Identify the blood parasite species.
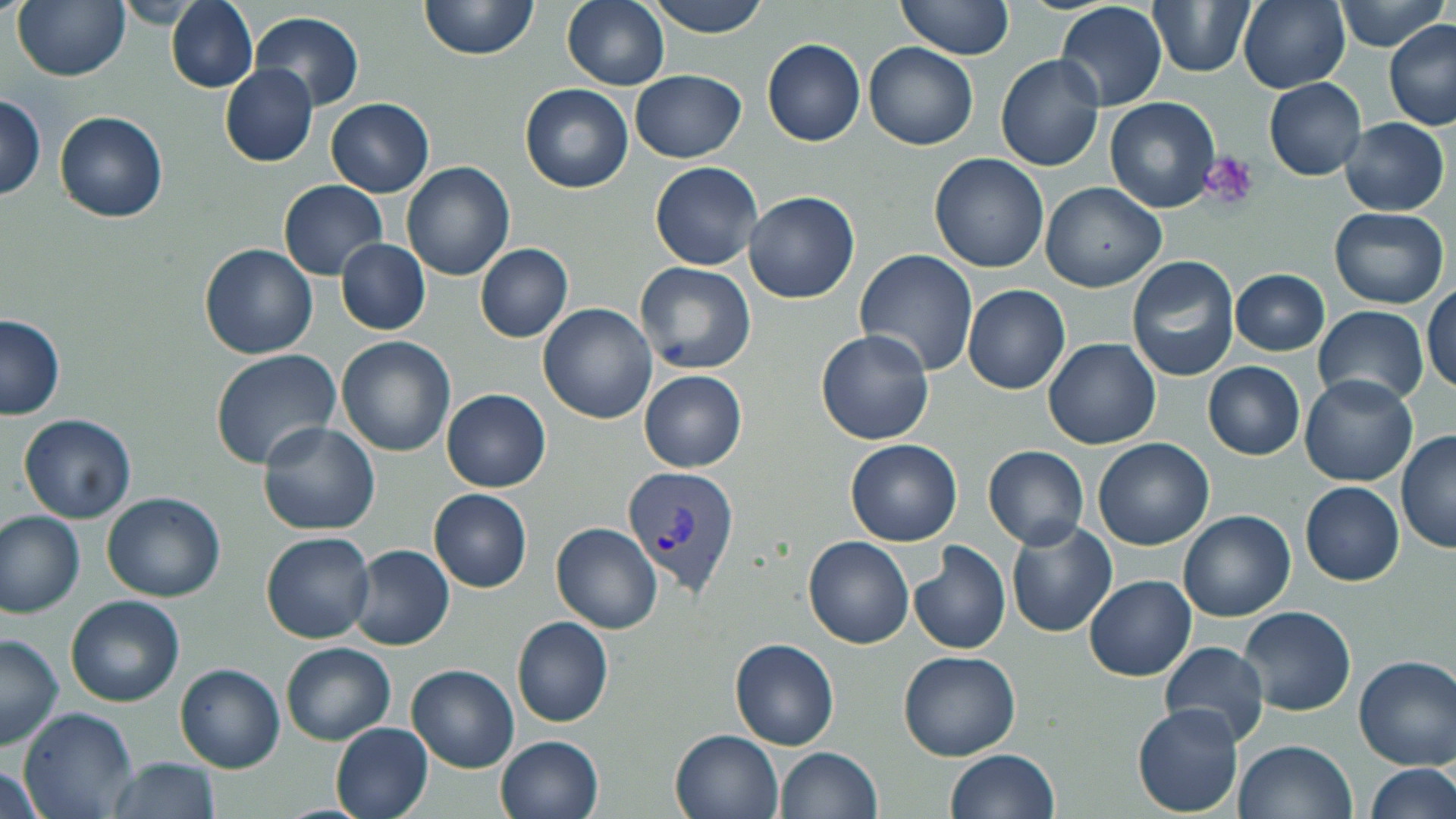
Plasmodium vivax.

Summary:
  - Coordinate format: approximate bounding boxes as (x1,y1)-(x2,y2) corner pairs in pixels
  - Plasmodium vivax-infected red blood cell locations: (624,463)-(742,598)
  - Platelet locations: (1197,152)-(1259,213)
  - Uninfected red blood cell locations: (13,0)-(129,80), (168,0)-(257,91), (419,0)-(542,61), (640,0)-(772,38), (1055,0)-(1166,111), (1148,0)-(1256,78), (1239,0)-(1351,91), (1335,0)-(1447,52), (561,1)-(671,91), (893,1)-(1017,64), (118,2)-(198,28), (251,12)-(365,110), (1016,19)-(1144,147), (1385,20)-(1456,131), (762,38)-(866,147), (865,41)-(978,149), (996,55)-(1103,171), (220,65)-(320,166), (631,68)-(747,162), (1263,77)-(1368,180), (520,84)-(634,194), (0,92)-(48,202), (1104,96)-(1221,213), (325,97)-(434,198), (54,111)-(169,223), (1339,116)-(1449,215), (929,153)-(1049,274), (650,161)-(764,271), (404,162)-(515,281), (279,179)-(388,278), (1041,182)-(1165,290), (744,190)-(860,304), (1328,206)-(1449,306), (336,238)-(430,334), (199,243)-(318,359), (475,243)-(574,342), (854,249)-(979,376), (1127,255)-(1241,382), (635,262)-(756,375), (1230,268)-(1329,356), (963,284)-(1071,394), (1425,287)-(1455,398), (538,303)-(657,426), (1314,305)-(1428,406), (0,314)-(66,419), (816,329)-(934,445), (335,336)-(457,457), (1044,338)-(1161,450), (209,349)-(342,469), (1203,362)-(1306,460), (639,370)-(747,471), (1300,373)-(1418,488), (442,389)-(552,492), (20,414)-(137,524), (256,420)-(381,535), (1398,430)-(1454,557), (847,438)-(963,546), (1094,438)-(1213,548), (983,445)-(1089,548), (1299,480)-(1405,585), (429,489)-(533,593), (102,493)-(225,601), (1178,510)-(1294,623), (0,511)-(85,616), (1005,521)-(1118,637), (553,522)-(662,635), (261,532)-(375,642), (804,536)-(915,649), (911,541)-(1012,657), (350,545)-(456,650), (1085,575)-(1196,680), (65,594)-(183,707), (1239,607)-(1356,718), (511,616)-(614,727), (0,632)-(64,751), (729,639)-(841,750), (1159,640)-(1270,747), (281,642)-(396,744), (898,650)-(1021,761), (1354,655)-(1456,769), (176,663)-(285,772), (407,665)-(518,771), (1133,704)-(1245,815), (20,707)-(136,819), (331,723)-(433,819), (671,730)-(786,819), (495,735)-(604,819), (1235,739)-(1356,819), (775,747)-(883,819), (946,749)-(1059,819), (104,756)-(222,819), (0,762)-(48,819), (1365,762)-(1454,817)
  - Preparation: thin blood smear
  - Modality: optical microscopy
  - Image size: 1456×819 pixels
  - Field of view: single
  - Magnification: 1000x
  - Stain: May-Grünwald-Giemsa